Name the parasite shown.
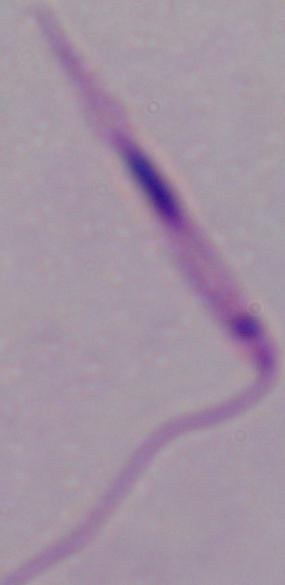
Leishmania.

Micrograph. Captured at 1000x magnification.